Locate every blood parasite and identify its species.
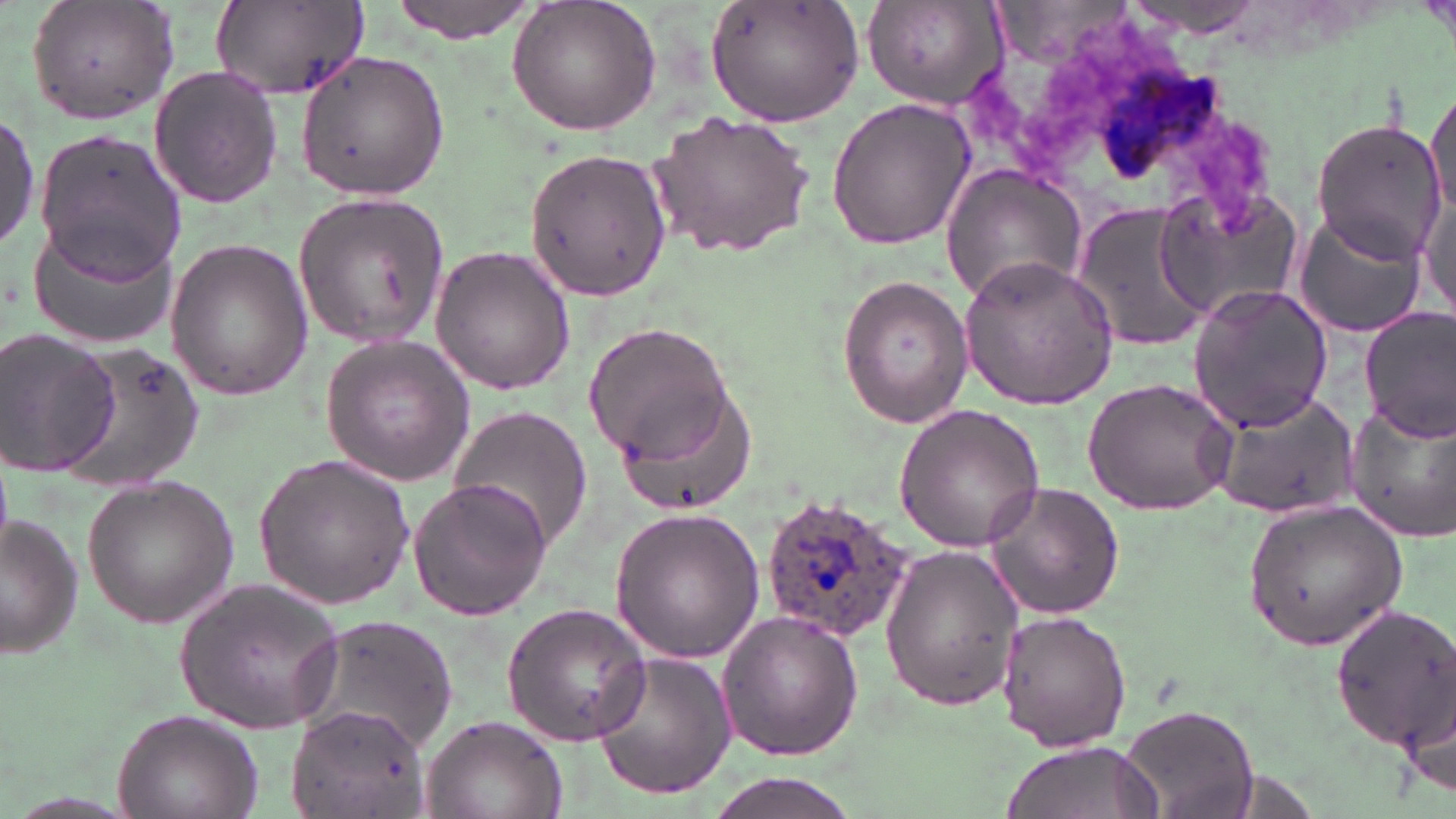
Approximate bounding boxes as (x1,y1)-(x2,y2) corner pairs in pixels.
Plasmodium ovale-infected red blood cells: (757,494)-(910,640).
No Plasmodium falciparum, Plasmodium malariae, Plasmodium vivax, Babesia divergens, or Trypanosoma brucei observed.

slide_level_diagnosis: Plasmodium ovale
uninfected_red_blood_cell_locations: 'approximate bounding boxes as (x1,y1)-(x2,y2) corner pairs in pixels: (24,0)-(181,126), (388,0)-(540,42), (506,0)-(663,137), (705,0)-(865,123), (863,0)-(1010,108), (209,2)-(367,101), (293,50)-(451,201), (148,64)-(283,209), (1426,79)-(1455,223), (827,97)-(975,249), (648,107)-(814,259), (1,111)-(39,256), (1310,116)-(1446,258), (33,130)-(188,285), (522,146)-(669,300), (940,164)-(1088,306), (1157,183)-(1304,319), (1420,183)-(1455,322), (293,188)-(449,348), (1071,200)-(1214,354), (1293,210)-(1428,337), (27,226)-(179,348), (164,238)-(314,402), (429,245)-(576,395), (958,255)-(1119,410), (836,275)-(972,427), (1188,284)-(1334,434), (1359,307)-(1456,439), (582,323)-(734,460), (1,329)-(121,476), (321,334)-(478,486), (58,342)-(207,494), (611,376)-(751,507), (1081,376)-(1238,515), (1209,390)-(1360,520), (1343,399)-(1456,545), (893,403)-(1046,554), (446,406)-(593,552), (254,453)-(416,607), (82,474)-(239,626), (407,474)-(555,621), (981,481)-(1126,620), (1242,499)-(1408,651), (607,507)-(766,662), (1,514)-(81,656), (881,544)-(1027,707), (176,577)-(345,733), (500,602)-(653,746), (1329,602)-(1456,749), (994,607)-(1132,750), (717,609)-(864,760), (296,612)-(460,760), (589,650)-(735,800), (1401,653)-(1455,809), (284,703)-(428,818), (1120,704)-(1260,818), (112,706)-(262,819), (421,714)-(567,819), (1001,739)-(1166,819), (697,773)-(865,819)'
image_size: 1456×819 pixels
preparation: thin blood film
field_of_view: single
stain: May-Grünwald-Giemsa
modality: optical microscopy
magnification: 1000x